Identify the parasite.
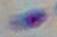

This is Toxoplasma gondii.

{
  "magnification": "1000x",
  "modality": "photomicrograph"
}